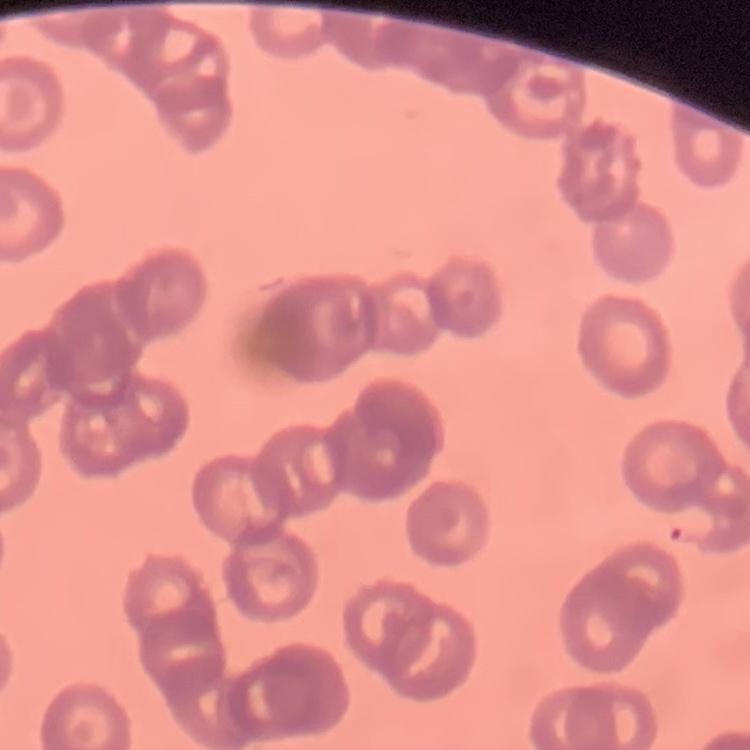

{
  "red_blood_cell_morphology": "rouleaux formation",
  "stain": "Field's or Giemsa",
  "image_type": "one tile cut from a larger photomicrograph",
  "preparation": "thin peripheral smear"
}